Report the malaria status of this cell.
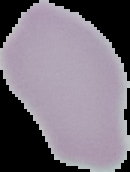

Uninfected.

From a thin blood film. Image is 130×172 pixels. Cell region segmented out of the field of view; the surrounding area is masked to black.